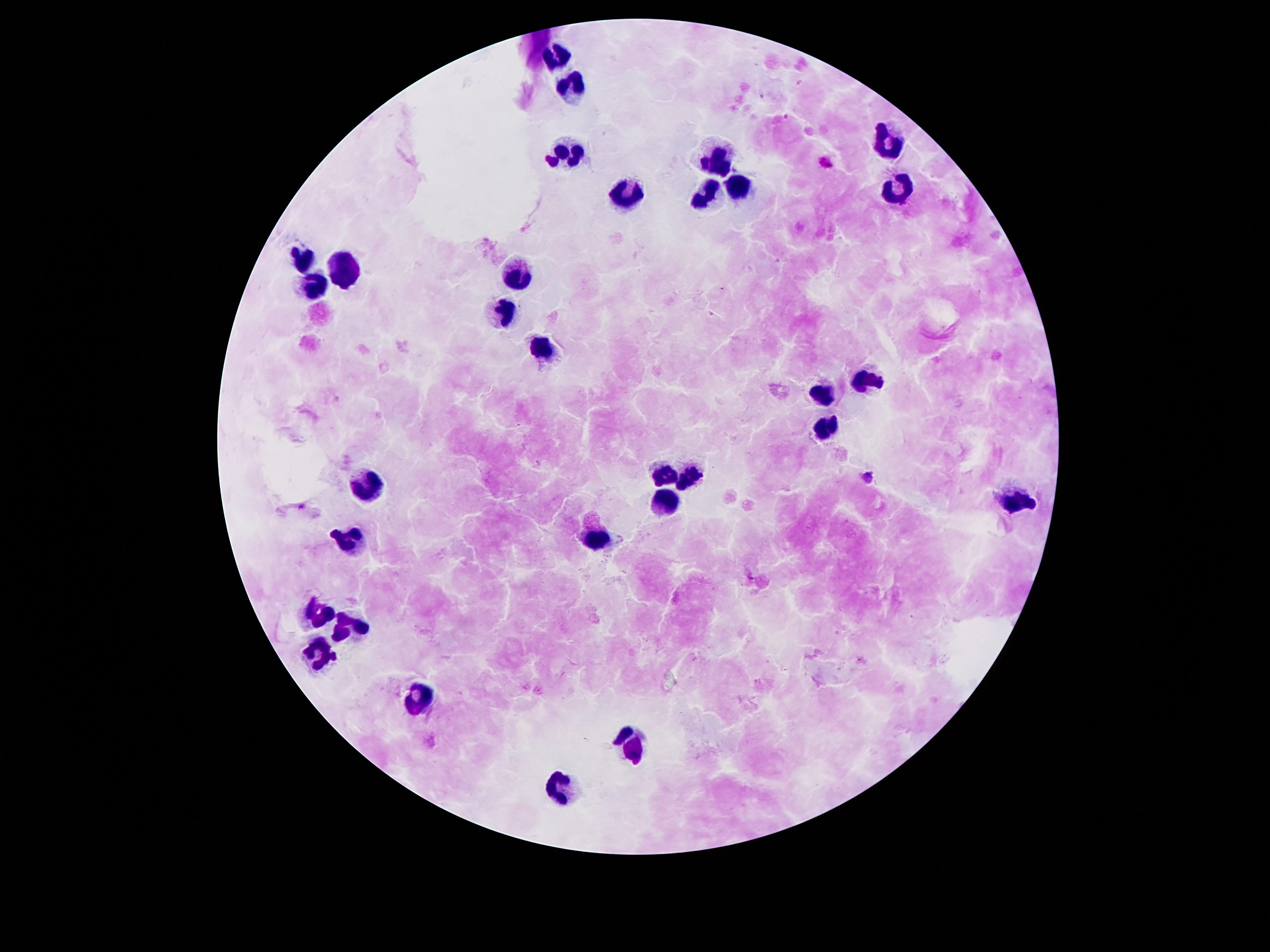

magnification: 100x
field_of_view: single
patient_malaria_status: positive for Plasmodium falciparum
stain: Giemsa
plasmodium_parasite_locations: 'approximate centers as {x, y} in pixels: {799, 82}, {763, 95}, {786, 117}, {539, 462}'
preparation: thick blood smear
leukocyte_locations: 'approximate centers as {x, y} in pixels: {555, 57}, {573, 90}, {887, 141}, {569, 156}, {718, 156}, {739, 187}, {897, 189}, {620, 194}, {709, 200}, {301, 261}, {520, 271}, {340, 274}, {312, 289}, {500, 312}, {543, 347}, {864, 381}, {820, 393}, {825, 429}, {665, 474}, {693, 475}, {363, 488}, {665, 497}, {1016, 505}, {597, 536}, {350, 539}, {316, 618}, {352, 623}, {319, 655}, {419, 699}, {635, 747}, {558, 790}'
capture: smartphone camera through the microscope eyepiece
image_size: 1270×952 pixels